Point out every malaria parasite.
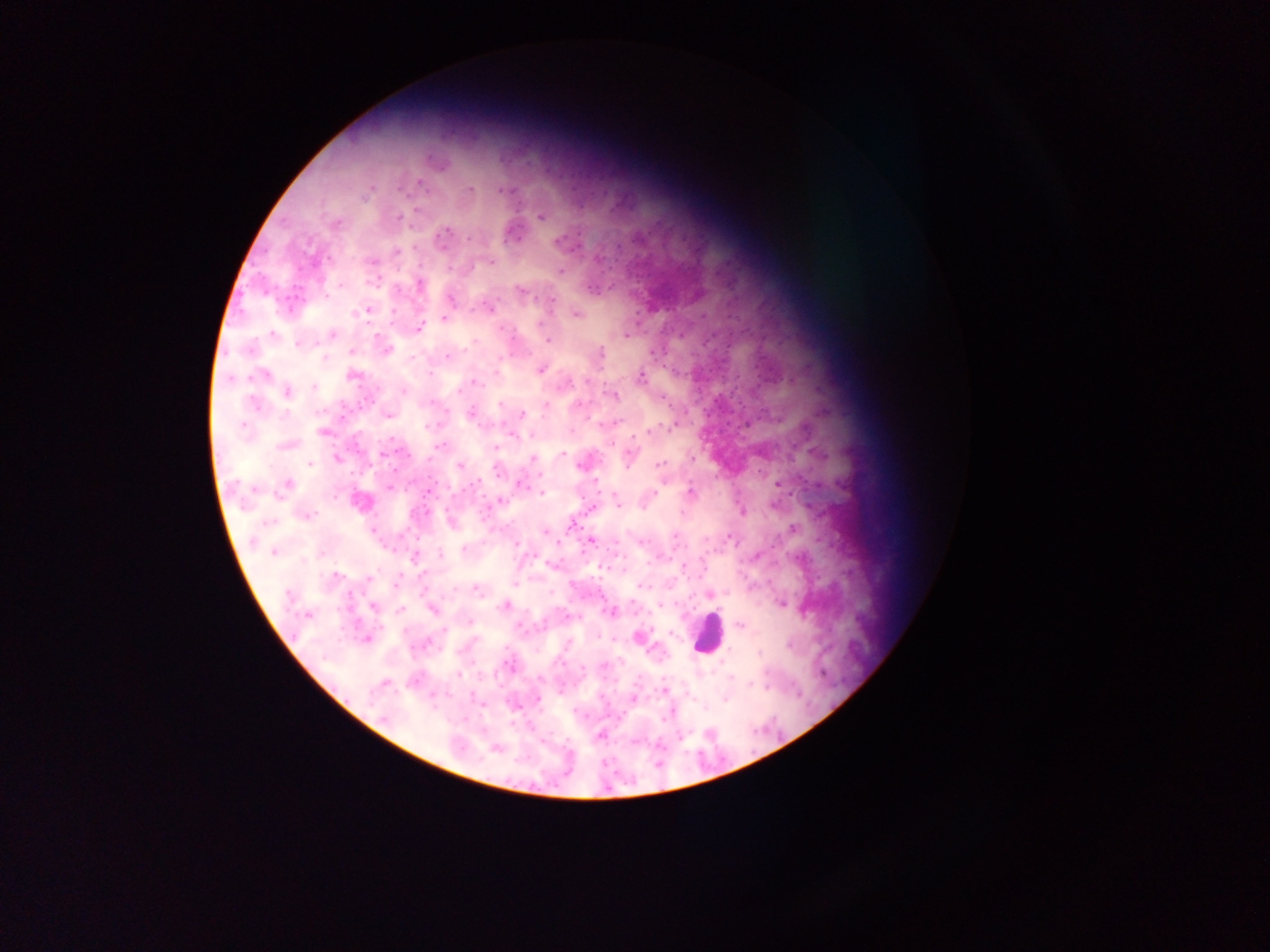

Approximate centers as {x, y} in pixels.
Malaria parasites: {437, 162}, {420, 182}, {470, 189}, {370, 190}, {502, 190}, {416, 209}, {540, 217}, {399, 218}, {337, 222}, {443, 237}, {470, 238}, {559, 242}, {396, 251}, {371, 261}, {491, 263}, {449, 268}, {561, 270}, {419, 283}, {591, 289}, {520, 291}, {553, 299}, {450, 300}, {489, 307}, {367, 310}, {356, 312}, {394, 313}, {577, 314}, {444, 318}, {540, 324}, {420, 328}, {273, 334}, {332, 335}, {627, 335}, {547, 339}, {472, 342}, {297, 345}, {469, 347}, {387, 349}, {352, 351}, {601, 353}, {448, 356}, {324, 358}, {413, 358}, {541, 370}, {264, 374}, {352, 375}, {641, 377}, {230, 379}, {586, 381}, {476, 383}, {566, 383}, {314, 387}, {403, 391}, {287, 392}, {614, 396}, {663, 399}, {254, 402}, {431, 402}, {500, 404}, {546, 405}, {578, 405}, {471, 413}, {388, 415}, {522, 415}, {243, 427}, {427, 427}, {671, 427}, {322, 431}, {647, 433}, {512, 435}, {287, 445}, {439, 446}, {385, 453}, {562, 454}, {628, 456}, {533, 458}, {693, 458}, {337, 459}, {310, 464}, {660, 464}, {461, 466}, {579, 466}, {498, 471}, {520, 484}, {777, 484}, {287, 485}, {389, 487}, {255, 489}, {690, 492}, {542, 493}, {654, 494}, {500, 501}, {360, 503}, {617, 503}, {742, 510}, {681, 513}, {308, 514}, {268, 522}, {793, 529}, {545, 533}, {675, 536}, {729, 537}, {591, 540}, {641, 541}, {516, 544}, {464, 548}, {274, 553}, {441, 554}, {756, 555}, {414, 558}, {337, 577}, {370, 578}, {514, 583}, {396, 584}, {642, 586}, {477, 589}, {710, 594}, {288, 596}, {781, 604}, {505, 605}, {661, 605}, {373, 607}, {401, 610}, {433, 610}, {610, 612}, {307, 616}, {568, 617}, {471, 621}, {738, 625}, {444, 629}, {671, 633}, {639, 637}, {568, 643}, {759, 652}, {603, 664}, {582, 669}, {459, 674}, {731, 678}, {540, 679}, {385, 683}, {750, 683}, {664, 691}, {538, 699}, {633, 699}, {725, 699}, {384, 717}, {681, 736}, {600, 737}, {495, 748}.

Leukocyte locations: {708, 632}. Image is 1270×952 pixels. Collected in Ghana. Single field of view. Photographed through a microscope with a mobile-phone camera. Thick blood film.